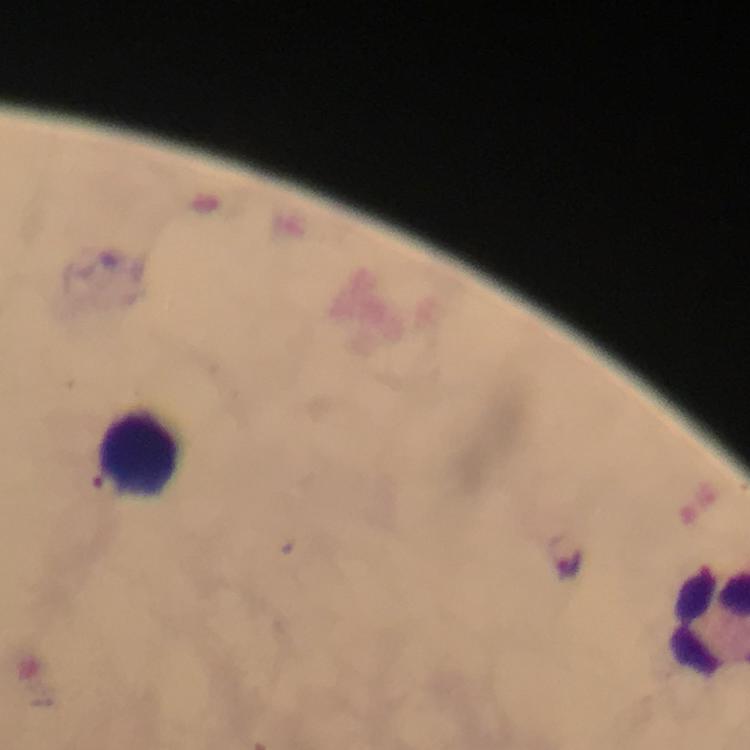

{
  "cropped_from": "one field of view",
  "immersion_oil": "used",
  "leukocyte_locations": "approximate centers as (x, y) in pixels: (138, 451)",
  "magnification": "100x",
  "preparation": "thick blood smear",
  "malaria_parasite_locations": "approximate centers as (x, y) in pixels: (570, 562)",
  "context": "from a diagnostic examination for malaria",
  "image_size": "750×750 pixels",
  "capture": "smartphone camera through the microscope",
  "stain": "Giemsa"
}